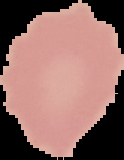
preparation: thin blood film
image_size: 124×160 pixels
image_type: cell region segmented out of the field of view; surrounding area masked to black
malaria_status: uninfected